Comment on the morphology of the red blood cells.
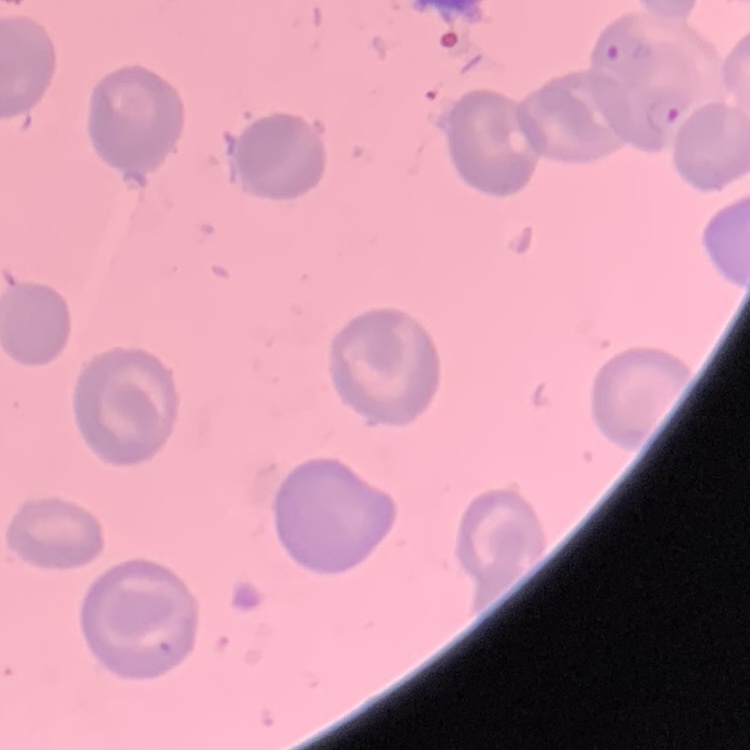

They show no rouleaux formation.

Square crop of a larger photomicrograph. Field's or Giemsa stain. Thin blood film.